Locate every Plasmodium parasite.
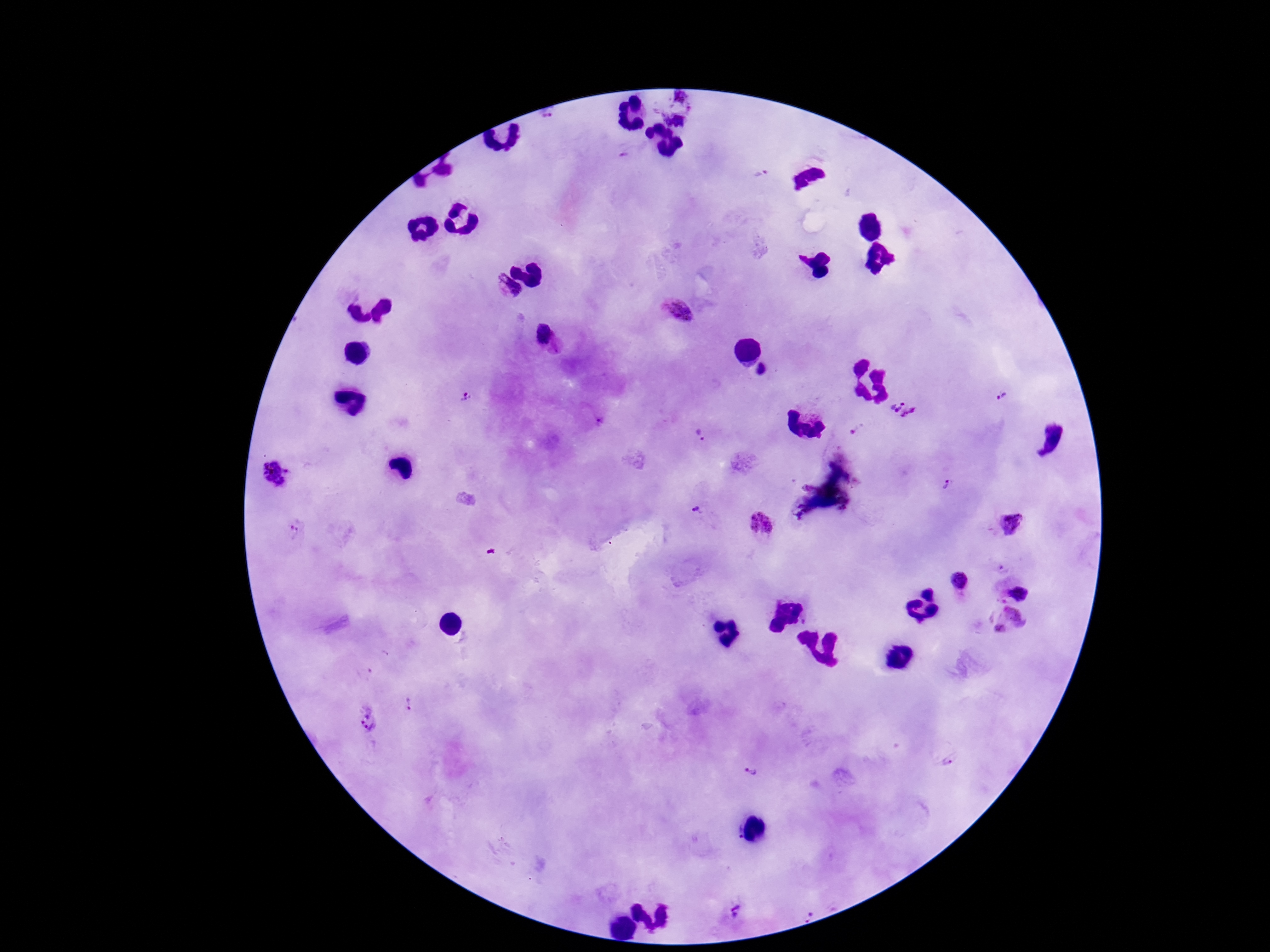

Approximate centers as [x, y] in pixels.
Plasmodium parasites: [547, 113], [759, 174], [505, 288], [680, 309], [544, 337], [764, 370], [466, 395], [1000, 397], [903, 409], [855, 428], [701, 434], [274, 473], [951, 485], [698, 509], [761, 522], [1010, 523], [295, 533], [1004, 567], [960, 581], [1018, 589], [1010, 620], [408, 704], [369, 720], [948, 759], [749, 777], [729, 909], [808, 910].

Summary:
  - Preparation: thick blood smear
  - Patient malaria status: positive
  - Image size: 1270×952 pixels
  - Stain: Giemsa
  - Capture: smartphone camera through the microscope eyepiece
  - Magnification: 100x
  - Field of view: single